Assess for Plasmodium parasites.
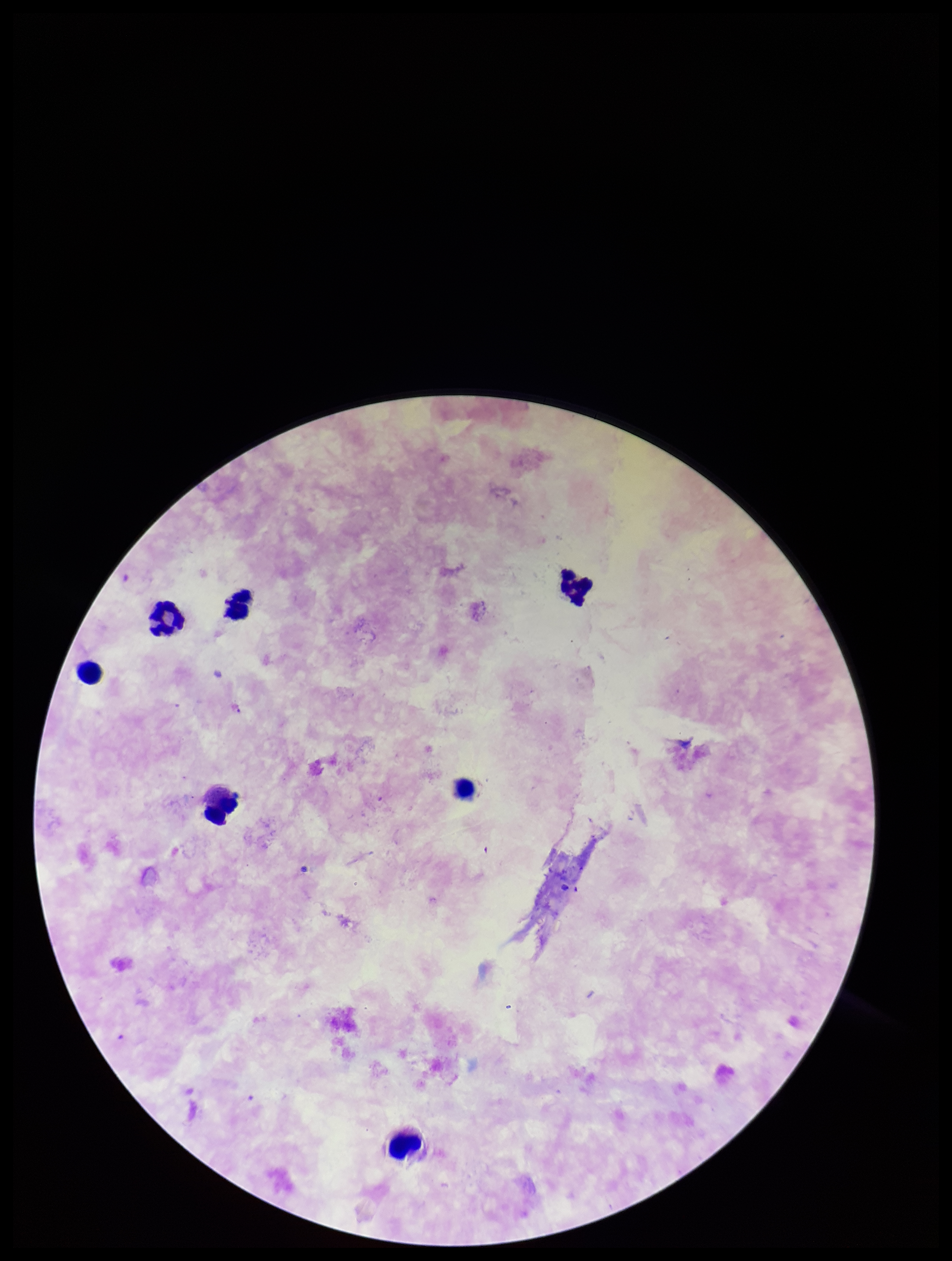
None identified.

Leukocyte count: 7. Image is 952×1261 pixels. Preparation: thick blood smear. Single field of view. Smartphone photograph taken through the eyepiece of a microscope. Patient malaria status: negative. Giemsa stain. Parasite count: 0.